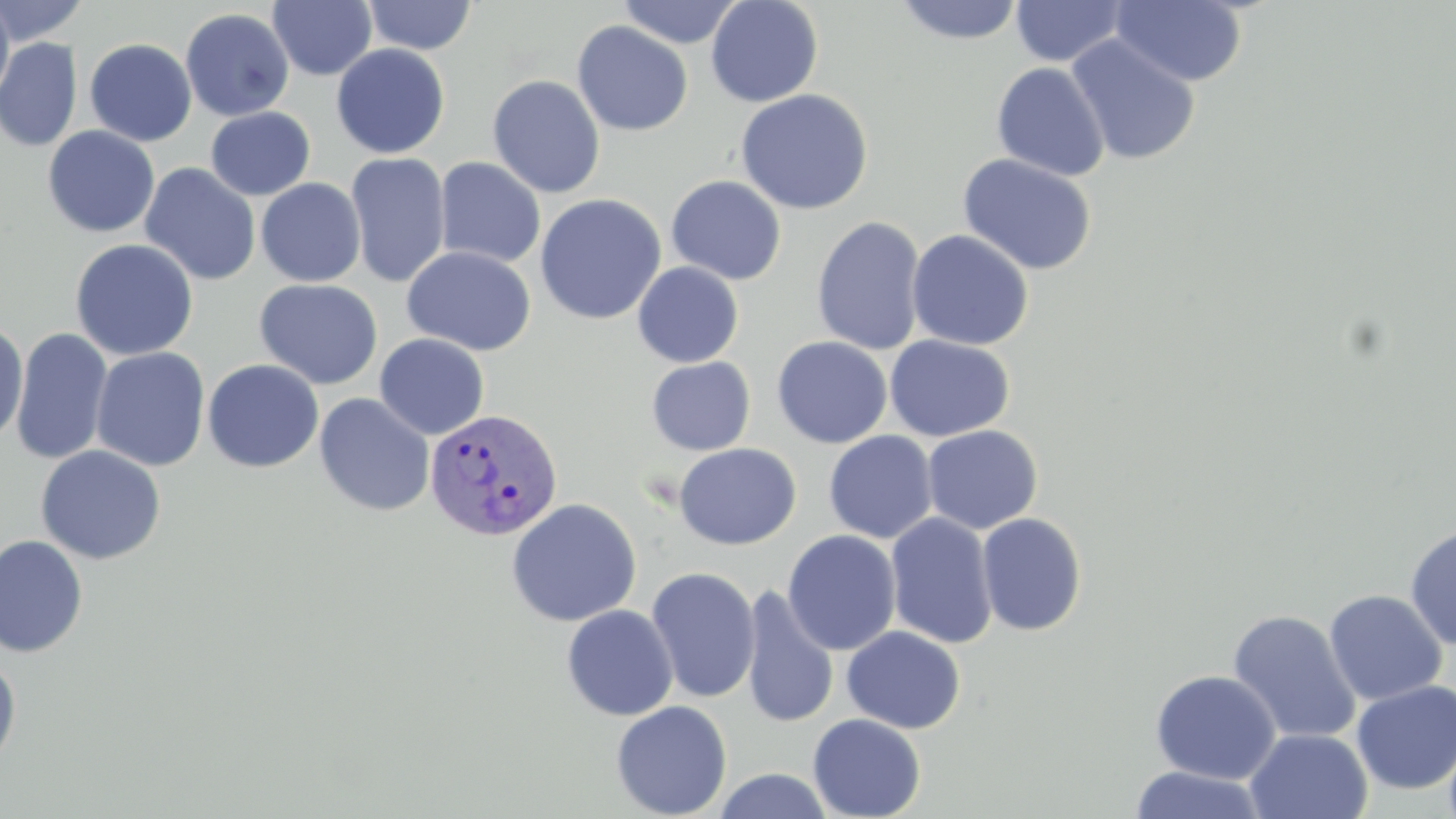
slide_level_diagnosis: Plasmodium vivax
image_size: 1456×819 pixels
stain: May-Grünwald-Giemsa
uninfected_red_blood_cell_locations: 'approximate bounding boxes as (x1,y1)-(x2,y2) corner pairs in pixels: (361,0)-(478,55), (617,0)-(743,48), (705,0)-(823,107), (1111,0)-(1248,87), (0,1)-(15,106), (0,1)-(92,45), (268,1)-(378,81), (893,1)-(1024,45), (1010,1)-(1129,67), (180,8)-(295,121), (572,21)-(694,136), (1066,33)-(1201,166), (0,38)-(83,152), (84,39)-(197,146), (331,43)-(450,158), (991,61)-(1110,181), (487,74)-(606,198), (735,89)-(873,214), (205,106)-(316,201), (42,126)-(160,238), (346,152)-(451,288), (957,153)-(1098,276), (434,157)-(546,268), (139,162)-(261,286), (666,175)-(787,285), (256,178)-(366,287), (535,193)-(667,325), (811,215)-(927,356), (906,229)-(1034,351), (70,239)-(199,361), (402,245)-(537,356), (632,262)-(744,367), (254,278)-(384,390), (0,320)-(28,448), (11,328)-(113,465), (374,333)-(490,440), (884,334)-(1015,441), (771,336)-(893,448), (91,347)-(211,472), (645,350)-(893,452), (646,356)-(756,456), (202,359)-(324,473), (314,393)-(435,517), (922,424)-(1043,534), (823,430)-(938,543), (674,443)-(801,550), (35,445)-(166,565), (505,498)-(642,627), (885,512)-(999,648), (977,512)-(1087,636), (1404,525)-(1456,651), (782,529)-(902,656), (0,534)-(88,658), (645,566)-(761,703), (741,585)-(839,729), (1324,589)-(1448,706), (561,604)-(679,721), (1227,609)-(1361,744), (841,626)-(966,733), (0,655)-(22,771), (1150,670)-(1281,783), (1351,680)-(1456,794), (610,700)-(732,818), (808,714)-(926,819), (1244,727)-(1373,819), (1128,765)-(1267,819), (710,768)-(836,819)'
preparation: thin blood smear
modality: light microscopy
plasmodium_vivax_infected_red_blood_cell_locations: 'approximate bounding boxes as (x1,y1)-(x2,y2) corner pairs in pixels: (425,407)-(563,541)'
field_of_view: one of a larger specimen
magnification: 1000x